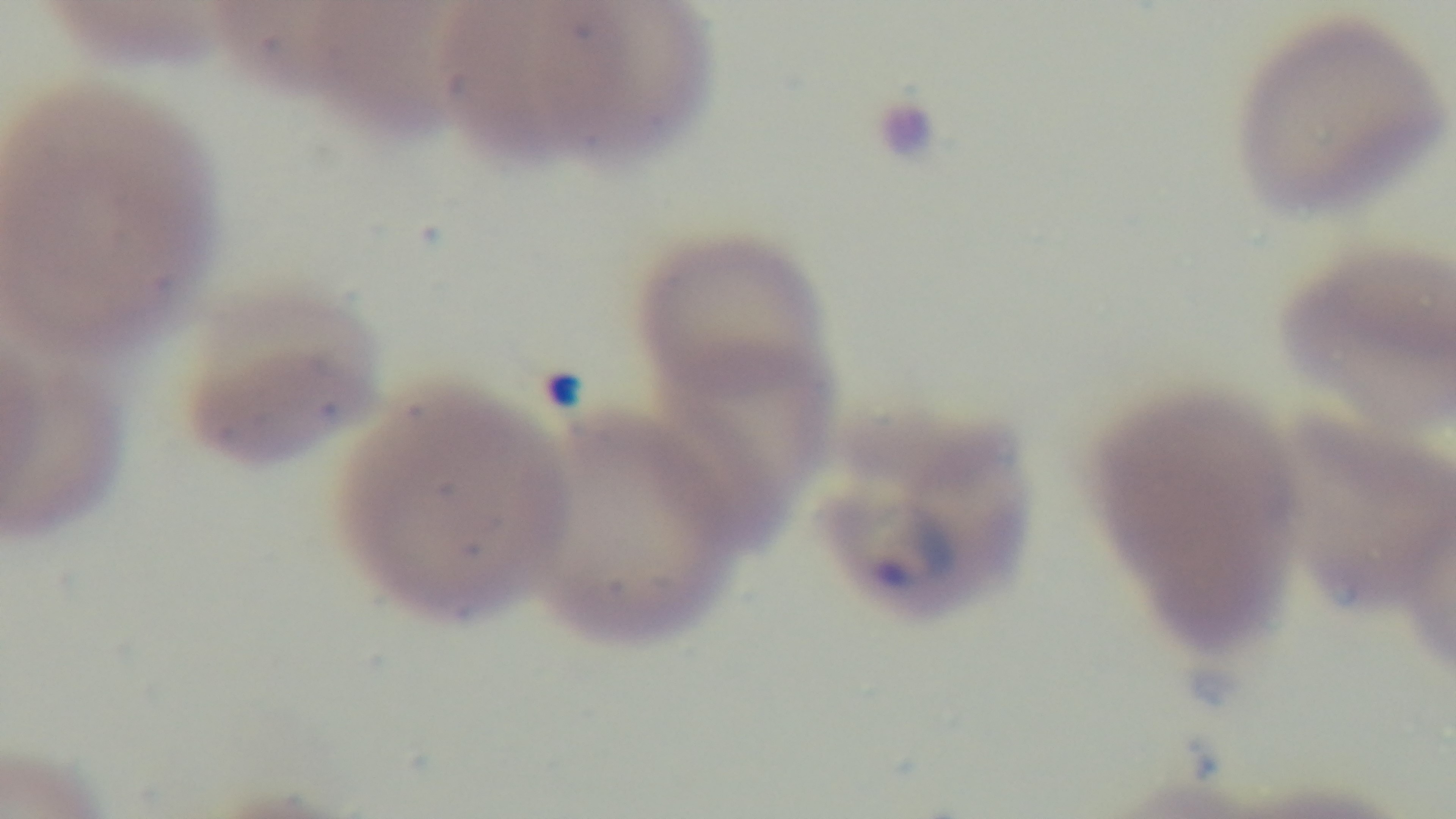

Giemsa-stained. Single field of view. Mounted 4K digital camera. Preparation: thin smear. Oil-immersion objective, 100x. Malaria status: infected. Light microscopy.